Report the malaria status of this cell.
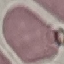
It is uninfected.

Summary:
  - Preparation: thin smear
  - Stain: Giemsa
  - Capture: smartphone camera at the microscope eyepiece
  - Image type: cell patch, automatically extracted from a larger field of view and resized to 64 × 64 pixels